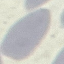

Summary:
  - Result: no malaria parasites detected
  - Stain: Giemsa
  - Image type: cell patch, automatically extracted from a larger field of view and resized to 64 × 64 pixels
  - Capture: smartphone through the microscope eyepiece
  - Preparation: thin blood film